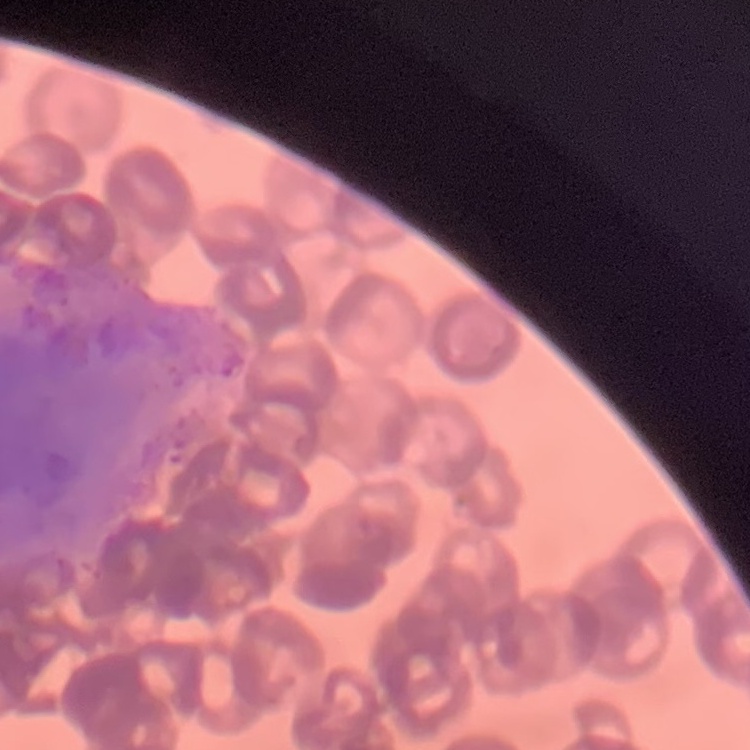
Summary:
  - Red blood cell morphology: rouleaux formation
  - Image type: square crop of a larger photomicrograph
  - Stain: Field's or Giemsa
  - Preparation: thin blood smear